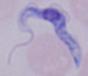
Summary:
  - Modality: micrograph
  - Magnification: 1000x
  - Identification: trypanosome